Identify the blood parasite species.
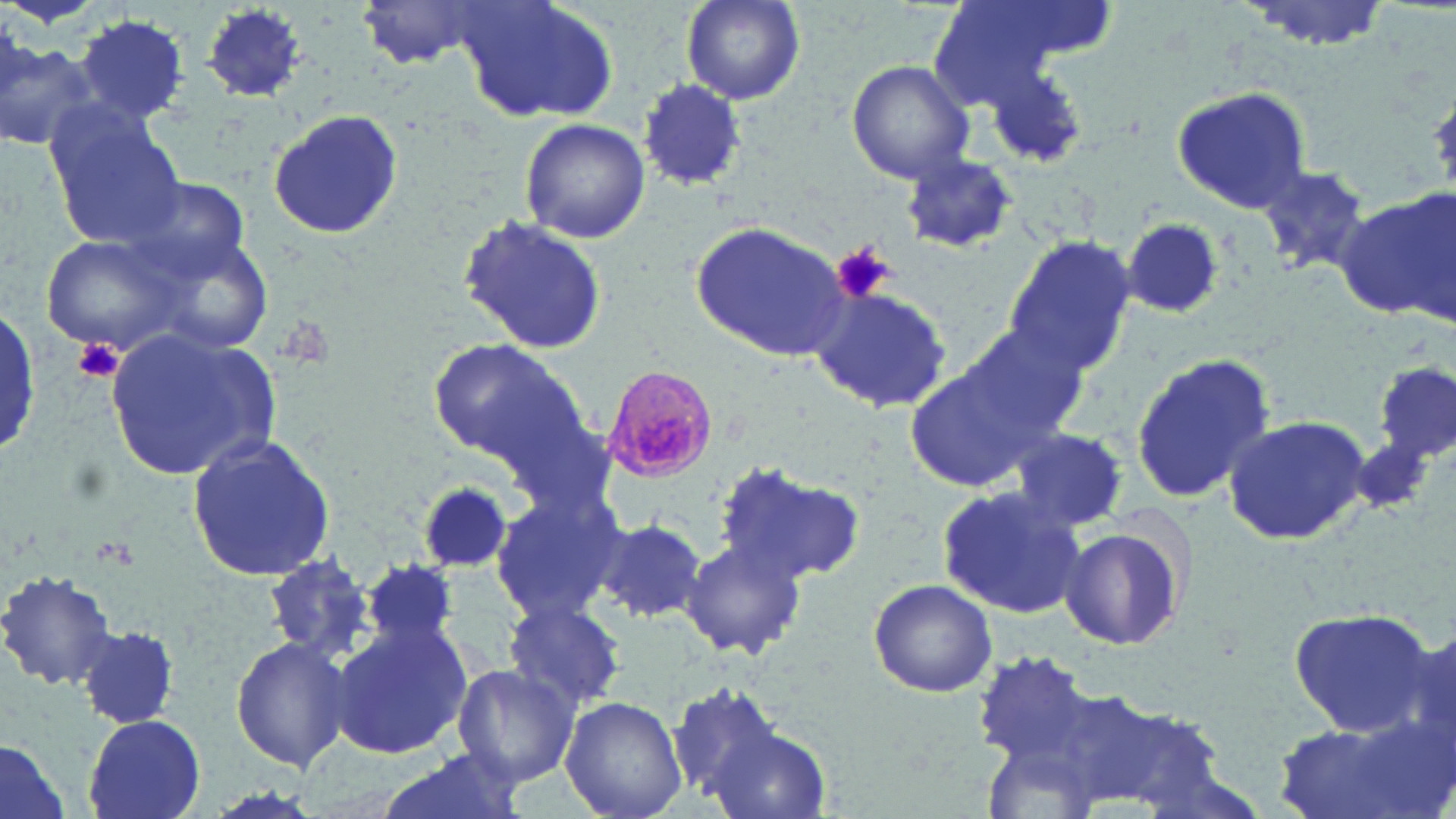

Plasmodium malariae.

Approximate bounding boxes as (x1, y1, x2, y2) in pixels. Plasmodium malariae-infected red blood cell locations: (601, 365, 717, 485). Platelet locations: (831, 242, 895, 305), (72, 337, 123, 384). Uninfected red blood cell locations: (355, 0, 494, 70), (455, 0, 622, 122), (679, 0, 806, 107), (925, 0, 1076, 107), (969, 0, 1116, 71), (1235, 0, 1397, 52), (197, 3, 308, 104), (75, 14, 191, 126), (0, 27, 97, 153), (846, 58, 977, 183), (977, 59, 1093, 169), (637, 79, 748, 190), (1171, 87, 1315, 213), (46, 109, 187, 250), (264, 109, 408, 241), (519, 119, 651, 245), (897, 152, 1019, 255), (1256, 164, 1375, 277), (131, 177, 252, 283), (1332, 192, 1455, 322), (458, 216, 610, 359), (1122, 216, 1228, 320), (692, 222, 852, 360), (40, 231, 191, 357), (152, 234, 277, 356), (1005, 235, 1136, 373), (805, 285, 953, 415), (0, 308, 42, 461), (952, 321, 1092, 446), (107, 323, 279, 476), (428, 337, 589, 467), (1132, 352, 1277, 502), (900, 354, 1061, 491), (1377, 360, 1454, 468), (1219, 417, 1375, 544), (1006, 429, 1130, 532), (186, 434, 339, 580), (1350, 435, 1434, 523), (714, 459, 871, 585), (417, 481, 513, 575), (488, 487, 624, 623), (934, 487, 1088, 617), (592, 517, 707, 625), (1057, 522, 1189, 652), (677, 541, 807, 659), (261, 553, 378, 665), (364, 557, 461, 654), (0, 569, 119, 690), (867, 578, 997, 697), (503, 599, 626, 714), (1287, 609, 1436, 735), (326, 620, 473, 760), (80, 625, 180, 728), (230, 633, 352, 771), (961, 649, 1240, 818), (452, 663, 580, 789), (665, 680, 787, 804), (561, 696, 686, 819), (1267, 711, 1452, 819), (83, 715, 207, 819), (702, 722, 832, 819), (0, 742, 72, 819), (375, 749, 531, 819). Image is 1456×819 pixels. May-Grünwald-Giemsa stain. Thin blood film. Captured at 1000x magnification. Light microscopy. Single field of view.